Classify this cell by malaria status.
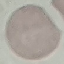

Uninfected.

Giemsa-stained preparation. Acquired by smartphone through the microscope eyepiece. Thin blood smear. Automatically extracted cell patch, resized to 64 × 64 pixels.